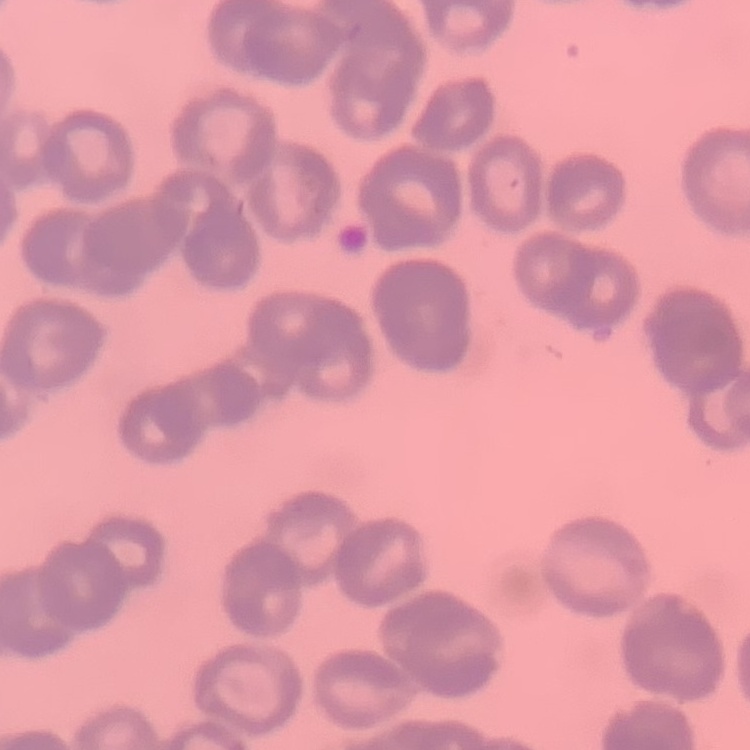
The red blood cells show rouleaux formation. Stained with either Field's or Giemsa. Square crop of a larger photomicrograph. Thin blood smear.